Comment on the morphology of the red blood cells.
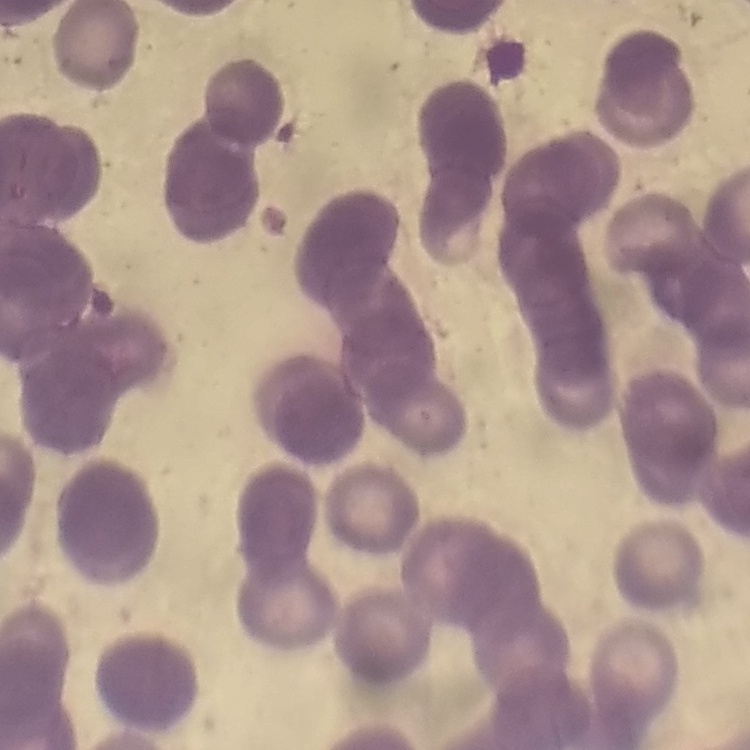

Rouleaux formation.

stain: Field's or Giemsa
image_type: one tile cut from a larger photomicrograph
preparation: thin blood film